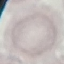 Result: negative for malaria parasites. Giemsa-stained preparation. Thin blood smear. Acquired by smartphone through the microscope eyepiece. Automatically extracted cell patch, resized to 64 × 64 pixels.